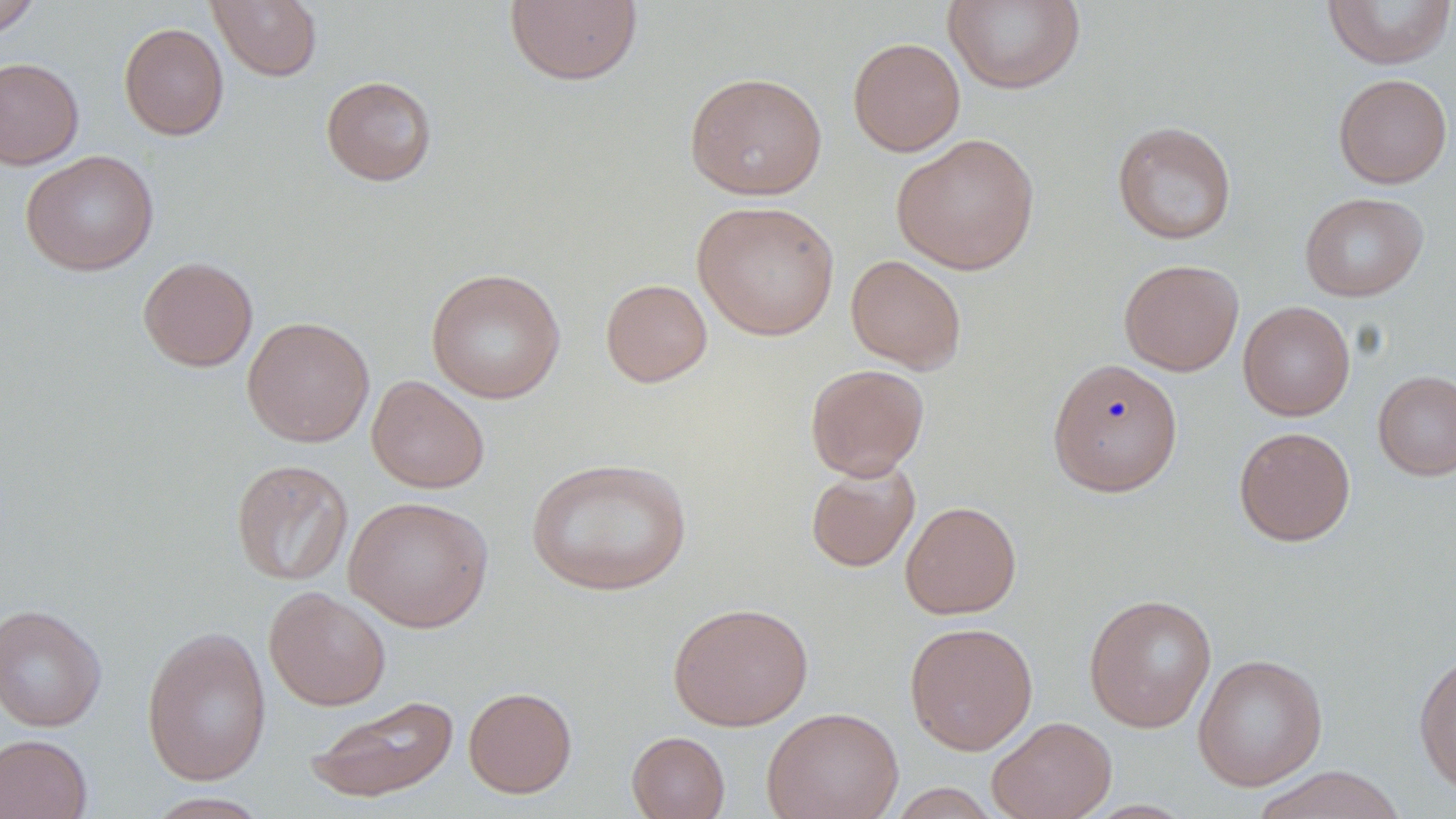

Approximate bounding boxes as (x1, y1, x2, y2) in pixels. Uninfected red blood cell locations: (207, 0, 323, 81), (504, 0, 643, 86), (944, 0, 1085, 94), (1322, 0, 1456, 69), (0, 1, 42, 39), (118, 22, 229, 140), (847, 37, 966, 157), (0, 58, 84, 170), (684, 71, 828, 200), (1333, 73, 1453, 189), (320, 75, 438, 186), (1111, 121, 1237, 244), (891, 133, 1041, 275), (20, 150, 159, 276), (1299, 191, 1429, 302), (692, 200, 840, 341), (845, 254, 967, 373), (138, 256, 258, 372), (1119, 259, 1244, 376), (425, 267, 566, 404), (600, 278, 712, 387), (1238, 301, 1355, 421), (242, 316, 375, 447), (1047, 358, 1184, 497), (805, 363, 930, 480), (1372, 370, 1456, 481), (367, 375, 489, 494), (1234, 426, 1356, 546), (525, 457, 693, 596), (231, 458, 354, 586), (805, 461, 920, 572), (344, 495, 494, 632), (900, 501, 1021, 619), (264, 586, 391, 710), (1083, 593, 1217, 732), (667, 602, 813, 730), (0, 604, 107, 731), (904, 621, 1038, 755), (141, 625, 272, 786), (1413, 651, 1456, 797), (1192, 653, 1328, 791), (463, 686, 577, 798), (303, 694, 459, 804), (761, 706, 904, 819), (987, 715, 1117, 819), (626, 731, 730, 819), (0, 733, 93, 819), (1250, 766, 1408, 819), (887, 783, 1003, 818), (142, 792, 273, 818). Slide-level diagnosis: no evidence of blood parasites. Optical microscopy. Captured at 1000x magnification. Image is 1456×819 pixels. May-Grünwald-Giemsa stain. One field of a larger specimen. Thin blood smear.